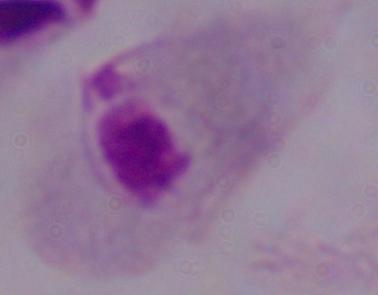 1000x magnification. A trichomonad is seen. Micrograph.